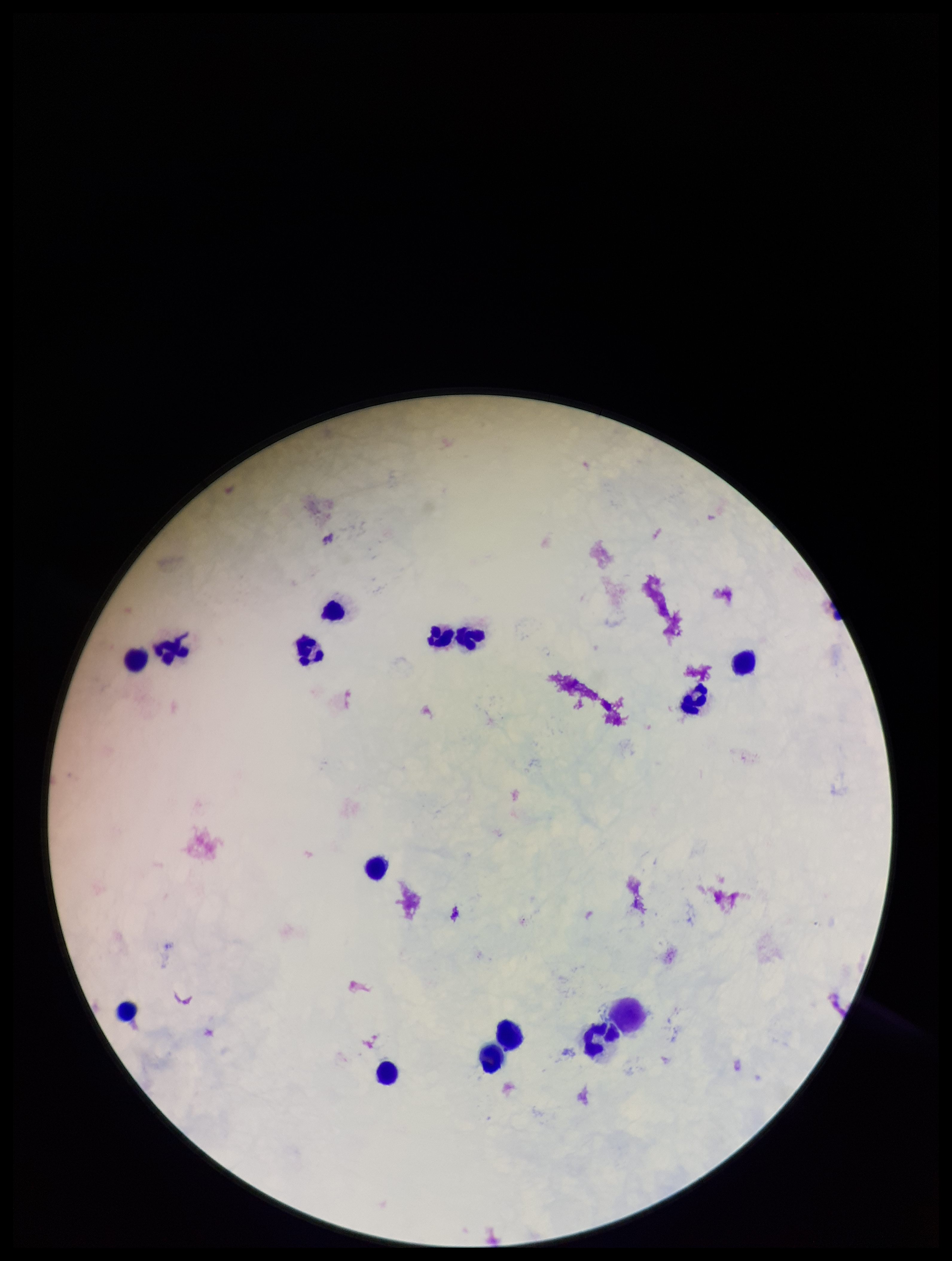
Parasite count: 0. One field from this slide. Plasmodium parasites: none identified. Smartphone photograph taken through the eyepiece of a microscope. Stained with Giemsa. Patient malaria status: negative. Image is 952×1261 pixels. Leukocyte count: 15. Preparation: thick blood smear.